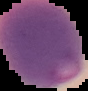
image type = segmented cell region with the area outside set to black
malaria status = parasitized
image size = 88×91 pixels
preparation = thin blood smear